State which parasite is depicted.
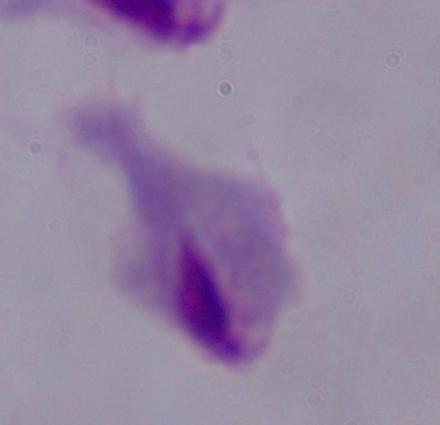
This is a trichomonad.

modality: micrograph
magnification: 1000x